Identify the cell.
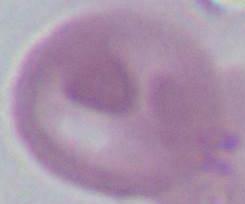
An erythrocyte.

Summary:
  - Modality: photomicrograph
  - Magnification: 1000x